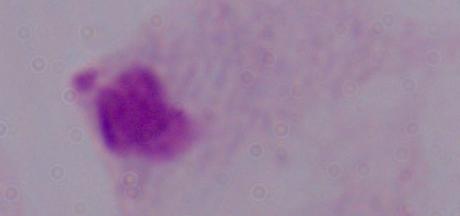
magnification = 1000x
identification = trichomonad
modality = micrograph